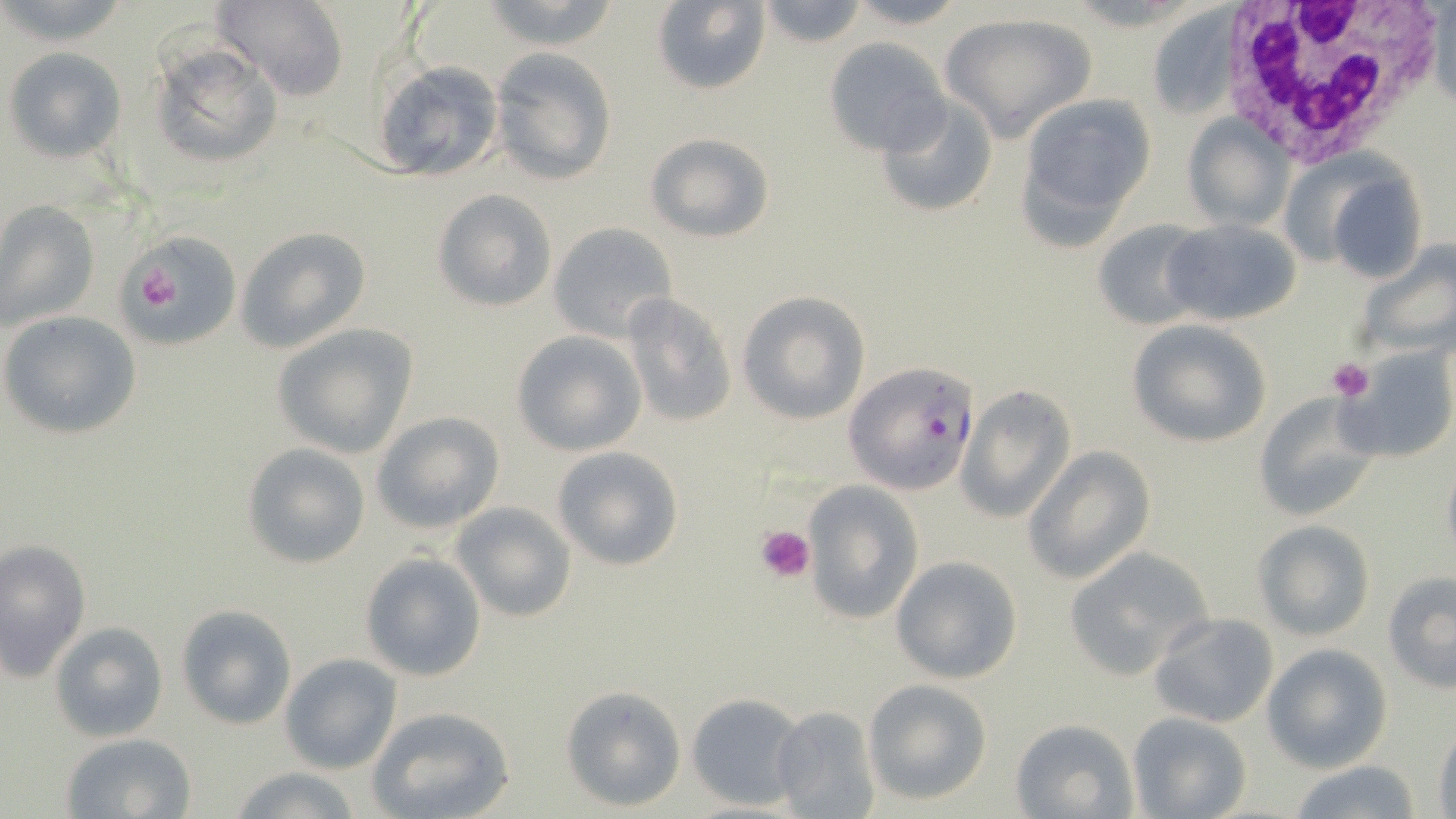
Summary:
  - Coordinate format: approximate bounding boxes as named x1/y1/x2/y2 corners in pixels
  - Platelet locations: (x1=129, y1=256, x2=189, y2=317), (x1=1326, y1=357, x2=1375, y2=401), (x1=755, y1=523, x2=816, y2=582)
  - White blood cell locations: (x1=1211, y1=0, x2=1448, y2=167)
  - Uninfected red blood cell locations: (x1=1, y1=0, x2=132, y2=45), (x1=213, y1=0, x2=349, y2=101), (x1=478, y1=0, x2=626, y2=50), (x1=756, y1=0, x2=869, y2=49), (x1=844, y1=0, x2=969, y2=29), (x1=649, y1=1, x2=772, y2=95), (x1=1146, y1=8, x2=1239, y2=120), (x1=939, y1=12, x2=1098, y2=141), (x1=824, y1=38, x2=951, y2=157), (x1=147, y1=43, x2=284, y2=171), (x1=3, y1=46, x2=127, y2=163), (x1=490, y1=47, x2=617, y2=186), (x1=370, y1=59, x2=506, y2=183), (x1=1016, y1=93, x2=1157, y2=232), (x1=874, y1=95, x2=998, y2=218), (x1=1182, y1=115, x2=1292, y2=231), (x1=644, y1=132, x2=775, y2=243), (x1=1317, y1=168, x2=1429, y2=284), (x1=433, y1=190, x2=559, y2=312), (x1=0, y1=200, x2=98, y2=333), (x1=1159, y1=218, x2=1301, y2=326), (x1=1092, y1=219, x2=1213, y2=332), (x1=546, y1=222, x2=677, y2=343), (x1=236, y1=226, x2=371, y2=354), (x1=121, y1=230, x2=243, y2=352), (x1=1352, y1=241, x2=1456, y2=362), (x1=737, y1=290, x2=871, y2=425), (x1=619, y1=292, x2=737, y2=429), (x1=2, y1=311, x2=142, y2=438), (x1=1127, y1=320, x2=1272, y2=447), (x1=272, y1=325, x2=416, y2=458), (x1=511, y1=330, x2=646, y2=457), (x1=1338, y1=345, x2=1454, y2=462), (x1=956, y1=384, x2=1077, y2=523), (x1=1252, y1=391, x2=1383, y2=523), (x1=371, y1=411, x2=505, y2=535), (x1=242, y1=443, x2=370, y2=569), (x1=550, y1=444, x2=687, y2=571), (x1=1024, y1=446, x2=1156, y2=584), (x1=1441, y1=457, x2=1456, y2=567), (x1=801, y1=481, x2=924, y2=628), (x1=450, y1=501, x2=577, y2=623), (x1=1252, y1=520, x2=1376, y2=640), (x1=1, y1=539, x2=91, y2=681), (x1=1063, y1=547, x2=1215, y2=678), (x1=359, y1=552, x2=488, y2=681), (x1=890, y1=555, x2=1023, y2=683), (x1=1382, y1=573, x2=1456, y2=692), (x1=176, y1=604, x2=296, y2=730), (x1=1149, y1=611, x2=1281, y2=730), (x1=49, y1=622, x2=168, y2=744), (x1=1263, y1=644, x2=1392, y2=772), (x1=281, y1=654, x2=401, y2=774), (x1=863, y1=678, x2=993, y2=805), (x1=559, y1=685, x2=688, y2=811), (x1=685, y1=691, x2=807, y2=812), (x1=768, y1=704, x2=881, y2=819), (x1=366, y1=705, x2=516, y2=819), (x1=1128, y1=711, x2=1252, y2=819), (x1=1010, y1=717, x2=1138, y2=819), (x1=1432, y1=727, x2=1456, y2=819), (x1=62, y1=732, x2=196, y2=818), (x1=1283, y1=760, x2=1430, y2=818), (x1=228, y1=765, x2=365, y2=819)
  - Plasmodium falciparum-infected red blood cell locations: (x1=845, y1=362, x2=981, y2=494)
  - Slide-level diagnosis: Plasmodium falciparum
  - Field of view: single
  - Image size: 1456×819 pixels
  - Stain: May-Grünwald-Giemsa
  - Modality: light microscopy
  - Magnification: 1000x
  - Preparation: thin blood film